Give the preparation type.
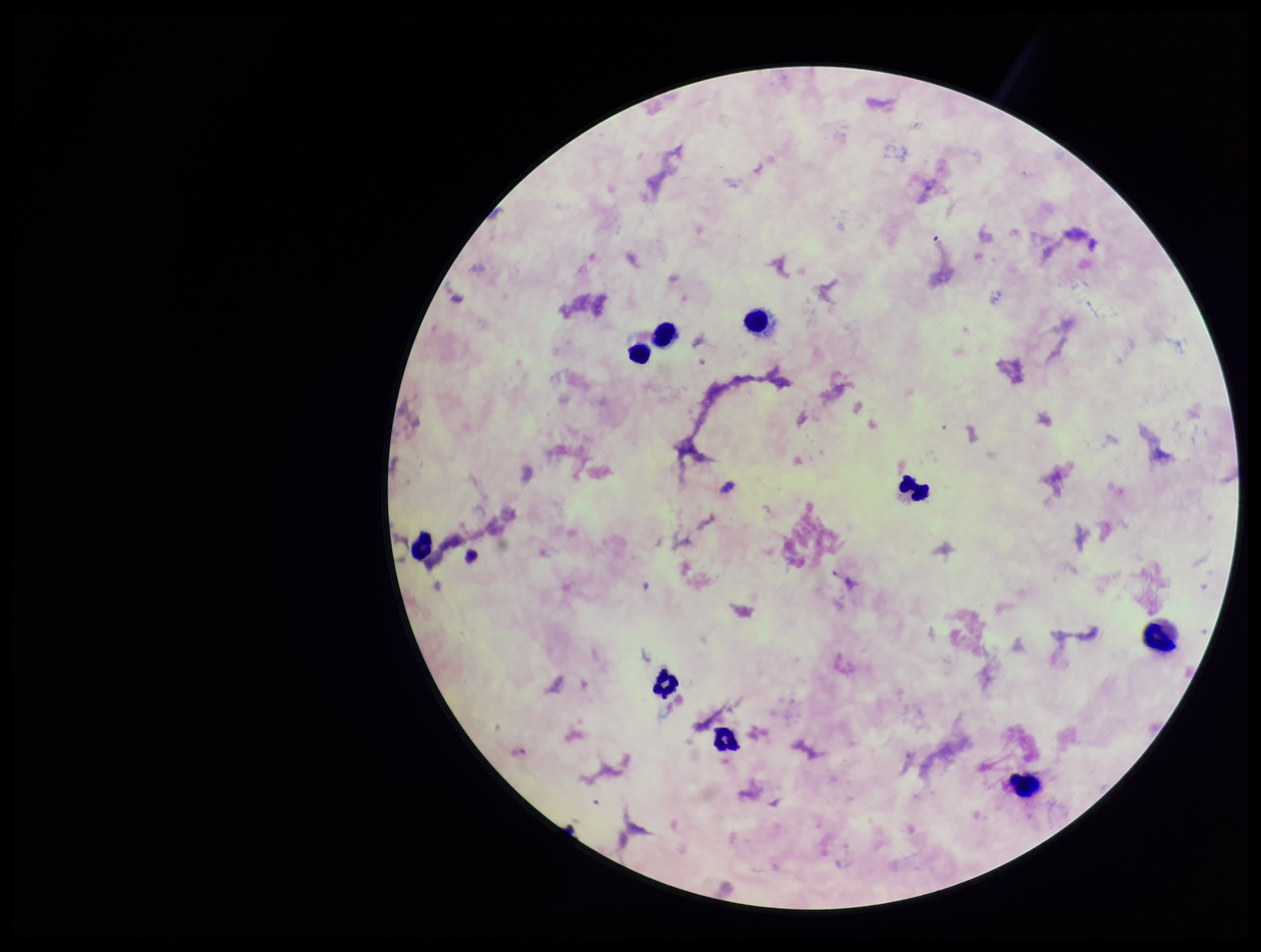
It is a thick blood smear.

Species reported for this patient: Plasmodium falciparum. Plasmodium parasites: none identified. Smartphone photograph taken through the eyepiece of a microscope. Leukocyte count: 9. Patient malaria status: positive. Image is 1261×952 pixels. Giemsa stain. Parasite count: 0. One field from this slide.